Identify the parasite.
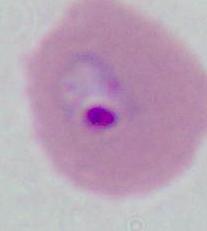

Plasmodium.

magnification: 400x or 1000x
modality: photomicrograph